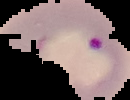
Image is 130×100 pixels. Result: malaria parasites identified. From a thin blood smear. Cell region segmented out of the field of view; the surrounding area is masked to black.